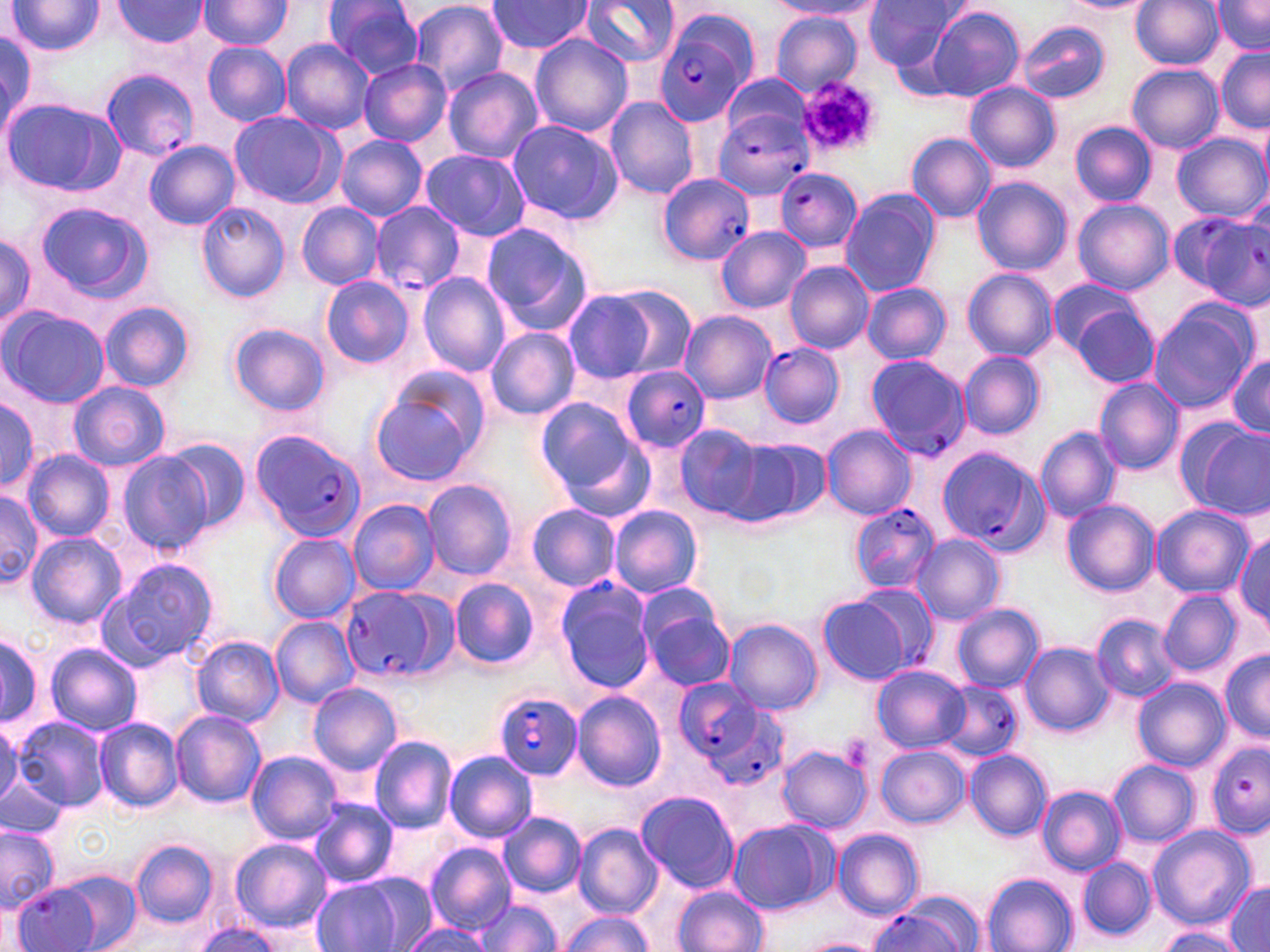

Approximate bounding boxes as named x1/y1/x2/y2 corners in pixels. Uninfected red blood cell locations: (x1=7, y1=0, x2=103, y2=56), (x1=323, y1=0, x2=424, y2=77), (x1=405, y1=0, x2=509, y2=95), (x1=864, y1=0, x2=960, y2=72), (x1=1130, y1=0, x2=1224, y2=71), (x1=1212, y1=0, x2=1270, y2=55), (x1=196, y1=1, x2=292, y2=50), (x1=485, y1=1, x2=592, y2=55), (x1=577, y1=1, x2=680, y2=69), (x1=768, y1=1, x2=877, y2=17), (x1=1059, y1=1, x2=1152, y2=12), (x1=114, y1=2, x2=209, y2=47), (x1=922, y1=5, x2=1024, y2=102), (x1=772, y1=12, x2=862, y2=96), (x1=1017, y1=21, x2=1111, y2=105), (x1=0, y1=30, x2=39, y2=134), (x1=531, y1=33, x2=633, y2=137), (x1=283, y1=40, x2=375, y2=134), (x1=202, y1=42, x2=291, y2=127), (x1=1215, y1=46, x2=1270, y2=131), (x1=359, y1=60, x2=451, y2=146), (x1=1128, y1=64, x2=1223, y2=152), (x1=442, y1=66, x2=542, y2=164), (x1=721, y1=72, x2=813, y2=148), (x1=965, y1=82, x2=1060, y2=172), (x1=605, y1=96, x2=699, y2=200), (x1=4, y1=98, x2=124, y2=196), (x1=230, y1=112, x2=335, y2=206), (x1=506, y1=119, x2=622, y2=225), (x1=1071, y1=122, x2=1158, y2=206), (x1=907, y1=132, x2=996, y2=223), (x1=1174, y1=133, x2=1268, y2=221), (x1=337, y1=135, x2=427, y2=222), (x1=145, y1=140, x2=240, y2=230), (x1=420, y1=149, x2=530, y2=241), (x1=379, y1=160, x2=506, y2=289), (x1=973, y1=176, x2=1071, y2=276), (x1=840, y1=188, x2=942, y2=298), (x1=1071, y1=199, x2=1175, y2=295), (x1=372, y1=201, x2=465, y2=294), (x1=35, y1=202, x2=149, y2=300), (x1=196, y1=202, x2=289, y2=303), (x1=296, y1=202, x2=384, y2=289), (x1=480, y1=220, x2=593, y2=333), (x1=717, y1=226, x2=811, y2=312), (x1=0, y1=233, x2=36, y2=331), (x1=786, y1=261, x2=874, y2=354), (x1=962, y1=269, x2=1057, y2=360), (x1=419, y1=273, x2=511, y2=377), (x1=321, y1=275, x2=413, y2=369), (x1=1046, y1=279, x2=1142, y2=359), (x1=862, y1=283, x2=951, y2=364), (x1=561, y1=285, x2=681, y2=385), (x1=101, y1=301, x2=195, y2=391), (x1=1148, y1=304, x2=1255, y2=413), (x1=1070, y1=305, x2=1162, y2=388), (x1=3, y1=306, x2=110, y2=407), (x1=681, y1=311, x2=775, y2=402), (x1=229, y1=323, x2=329, y2=415), (x1=485, y1=326, x2=580, y2=420), (x1=1228, y1=350, x2=1270, y2=440), (x1=959, y1=351, x2=1045, y2=439), (x1=1094, y1=377, x2=1185, y2=474), (x1=69, y1=380, x2=170, y2=471), (x1=368, y1=380, x2=481, y2=486), (x1=0, y1=397, x2=43, y2=491), (x1=534, y1=398, x2=640, y2=498), (x1=1184, y1=416, x2=1270, y2=518), (x1=674, y1=424, x2=766, y2=520), (x1=822, y1=426, x2=915, y2=519), (x1=1036, y1=426, x2=1122, y2=522), (x1=730, y1=438, x2=829, y2=526), (x1=166, y1=440, x2=251, y2=531), (x1=23, y1=450, x2=115, y2=542), (x1=118, y1=450, x2=213, y2=554), (x1=422, y1=479, x2=516, y2=579), (x1=0, y1=486, x2=43, y2=582), (x1=348, y1=499, x2=440, y2=595), (x1=1061, y1=501, x2=1160, y2=597), (x1=526, y1=503, x2=621, y2=593), (x1=1151, y1=504, x2=1254, y2=597), (x1=609, y1=505, x2=703, y2=598), (x1=1233, y1=530, x2=1270, y2=631), (x1=25, y1=532, x2=125, y2=628), (x1=269, y1=533, x2=360, y2=622), (x1=912, y1=535, x2=1004, y2=624), (x1=94, y1=559, x2=218, y2=671), (x1=451, y1=578, x2=539, y2=669), (x1=553, y1=578, x2=656, y2=695), (x1=856, y1=580, x2=940, y2=672), (x1=1159, y1=588, x2=1242, y2=676), (x1=817, y1=592, x2=914, y2=687), (x1=638, y1=597, x2=736, y2=692), (x1=951, y1=602, x2=1044, y2=692), (x1=270, y1=616, x2=358, y2=707), (x1=1092, y1=616, x2=1178, y2=699), (x1=724, y1=619, x2=820, y2=715), (x1=0, y1=630, x2=44, y2=732), (x1=192, y1=636, x2=284, y2=725), (x1=1019, y1=640, x2=1115, y2=736), (x1=45, y1=643, x2=141, y2=737), (x1=1220, y1=648, x2=1270, y2=741), (x1=871, y1=664, x2=970, y2=752), (x1=1133, y1=678, x2=1229, y2=771), (x1=308, y1=682, x2=402, y2=776), (x1=573, y1=691, x2=666, y2=790), (x1=169, y1=709, x2=265, y2=808), (x1=94, y1=716, x2=184, y2=814), (x1=13, y1=717, x2=108, y2=811), (x1=0, y1=724, x2=26, y2=812), (x1=369, y1=735, x2=457, y2=835), (x1=876, y1=744, x2=971, y2=828), (x1=777, y1=745, x2=871, y2=833), (x1=965, y1=749, x2=1052, y2=842), (x1=247, y1=751, x2=342, y2=844), (x1=444, y1=751, x2=537, y2=842), (x1=1110, y1=759, x2=1200, y2=848), (x1=0, y1=772, x2=66, y2=839), (x1=1037, y1=785, x2=1126, y2=875), (x1=637, y1=791, x2=738, y2=894), (x1=309, y1=797, x2=399, y2=888), (x1=499, y1=812, x2=586, y2=898), (x1=728, y1=820, x2=835, y2=913), (x1=574, y1=824, x2=662, y2=918), (x1=0, y1=825, x2=58, y2=912), (x1=1147, y1=825, x2=1256, y2=929), (x1=834, y1=828, x2=924, y2=922), (x1=131, y1=839, x2=219, y2=927), (x1=231, y1=839, x2=330, y2=932), (x1=425, y1=843, x2=515, y2=934), (x1=1075, y1=856, x2=1157, y2=941), (x1=49, y1=868, x2=143, y2=952), (x1=982, y1=873, x2=1078, y2=952), (x1=310, y1=875, x2=416, y2=951), (x1=1224, y1=880, x2=1270, y2=950), (x1=13, y1=881, x2=104, y2=952), (x1=674, y1=885, x2=769, y2=952), (x1=471, y1=897, x2=562, y2=951), (x1=556, y1=912, x2=656, y2=952), (x1=402, y1=921, x2=492, y2=952), (x1=191, y1=922, x2=284, y2=952), (x1=1152, y1=926, x2=1247, y2=952), (x1=798, y1=938, x2=884, y2=952). Platelet locations: (x1=796, y1=76, x2=878, y2=158), (x1=843, y1=733, x2=874, y2=771). Plasmodium falciparum-infected red blood cell locations: (x1=656, y1=22, x2=754, y2=126), (x1=102, y1=67, x2=198, y2=159), (x1=714, y1=112, x2=815, y2=200), (x1=775, y1=168, x2=863, y2=252), (x1=657, y1=173, x2=755, y2=263), (x1=1174, y1=209, x2=1269, y2=308), (x1=759, y1=342, x2=845, y2=428), (x1=865, y1=353, x2=971, y2=460), (x1=621, y1=367, x2=713, y2=452), (x1=249, y1=428, x2=368, y2=542), (x1=935, y1=445, x2=1047, y2=554), (x1=848, y1=503, x2=941, y2=594), (x1=340, y1=585, x2=454, y2=683), (x1=673, y1=678, x2=776, y2=776), (x1=938, y1=680, x2=1022, y2=763), (x1=492, y1=691, x2=585, y2=781), (x1=1207, y1=741, x2=1270, y2=835), (x1=876, y1=899, x2=975, y2=952). Slide-level diagnosis: Plasmodium falciparum. Light microscopy. 1000x magnification. Single field of view. Image is 1270×952 pixels. Thin blood film. May-Grünwald-Giemsa stain.